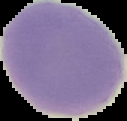 The area outside the segmented cell region is set to black. Malaria status: uninfected. Image is 127×121 pixels. From a thin blood smear.